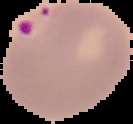

Malaria status: parasitized. Image is 133×124 pixels. Cell region segmented out of the field of view; the surrounding area is masked to black. From a thin blood film.